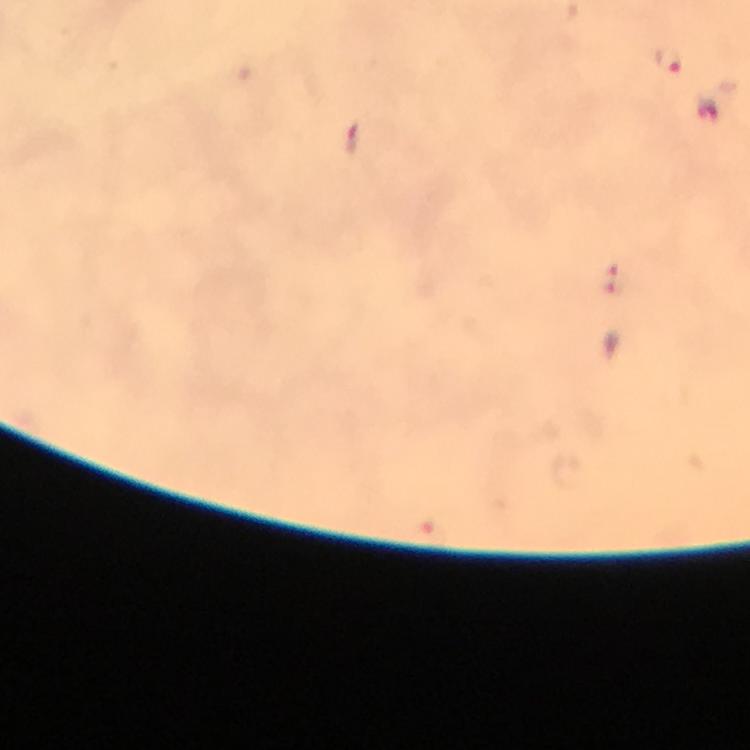
{
  "image_size": "750×750 pixels",
  "immersion_oil": "used",
  "context": "from a diagnostic examination for malaria",
  "capture": "smartphone mounted on the microscope",
  "cropped_from": "one field of view",
  "stain": "Giemsa",
  "malaria_parasite_locations": "approximate object centers, in pixels from the top-left corner: (x=668, y=63), (x=710, y=110), (x=353, y=139), (x=614, y=281)",
  "magnification": "100x",
  "preparation": "thick blood smear"
}